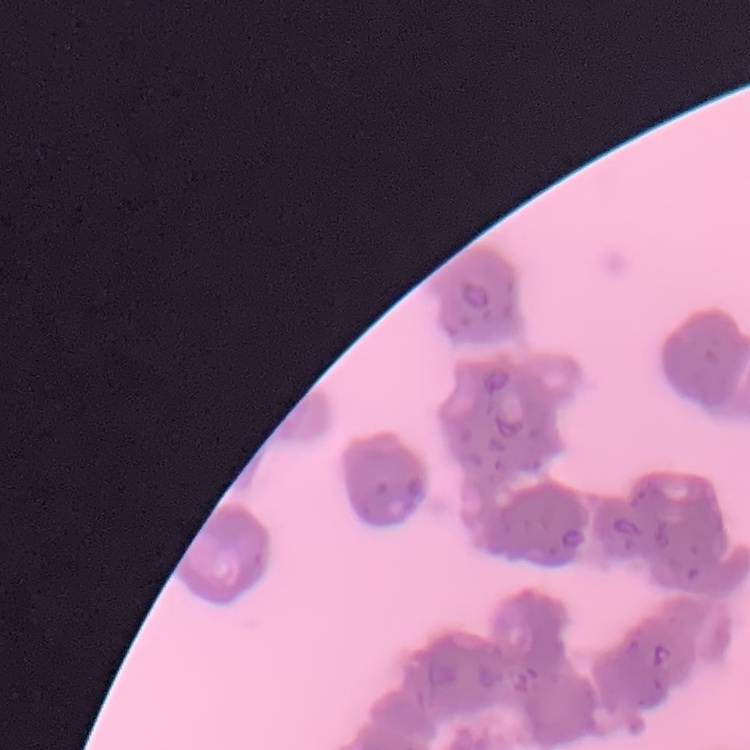

Summary:
  - Erythrocyte morphology: rouleaux formation
  - Preparation: thin peripheral smear
  - Image type: one tile cut from a larger photomicrograph
  - Stain: Field's or Giemsa